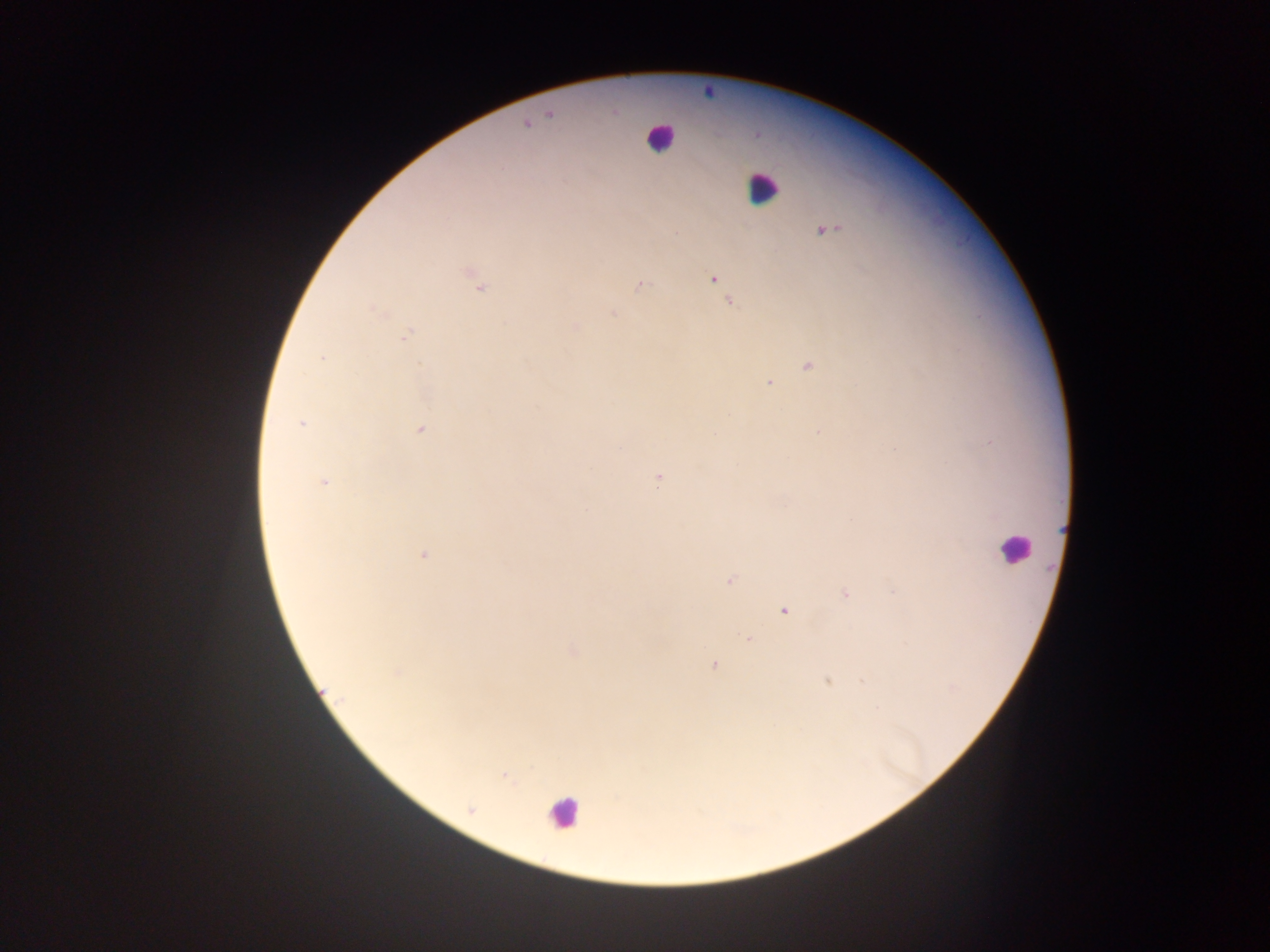 Approximate centers as x y in pixels. Leukocyte locations: 660 137; 761 187; 1015 549; 563 812. Plasmodium parasite locations: 551 114; 525 123; 824 229; 470 273; 712 279; 640 284; 479 287; 728 300; 378 310; 614 312; 576 327; 405 334; 321 358; 807 366; 769 383; 302 423; 420 430; 819 431; 659 478; 323 481; 424 554; 729 580; 846 593; 784 610; 749 638; 573 652; 714 664; 396 673; 828 679; 863 679; 323 694; 504 774; 471 809. Mobile-phone photograph taken through the microscope. One field of view. Image is 1270×952 pixels. Sample from Ghana. Thick blood smear.